Classify this cell by malaria status.
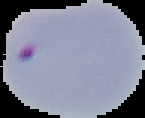

Parasitized.

From a thin blood smear. Image is 145×118 pixels. The area outside the segmented cell region is set to black.